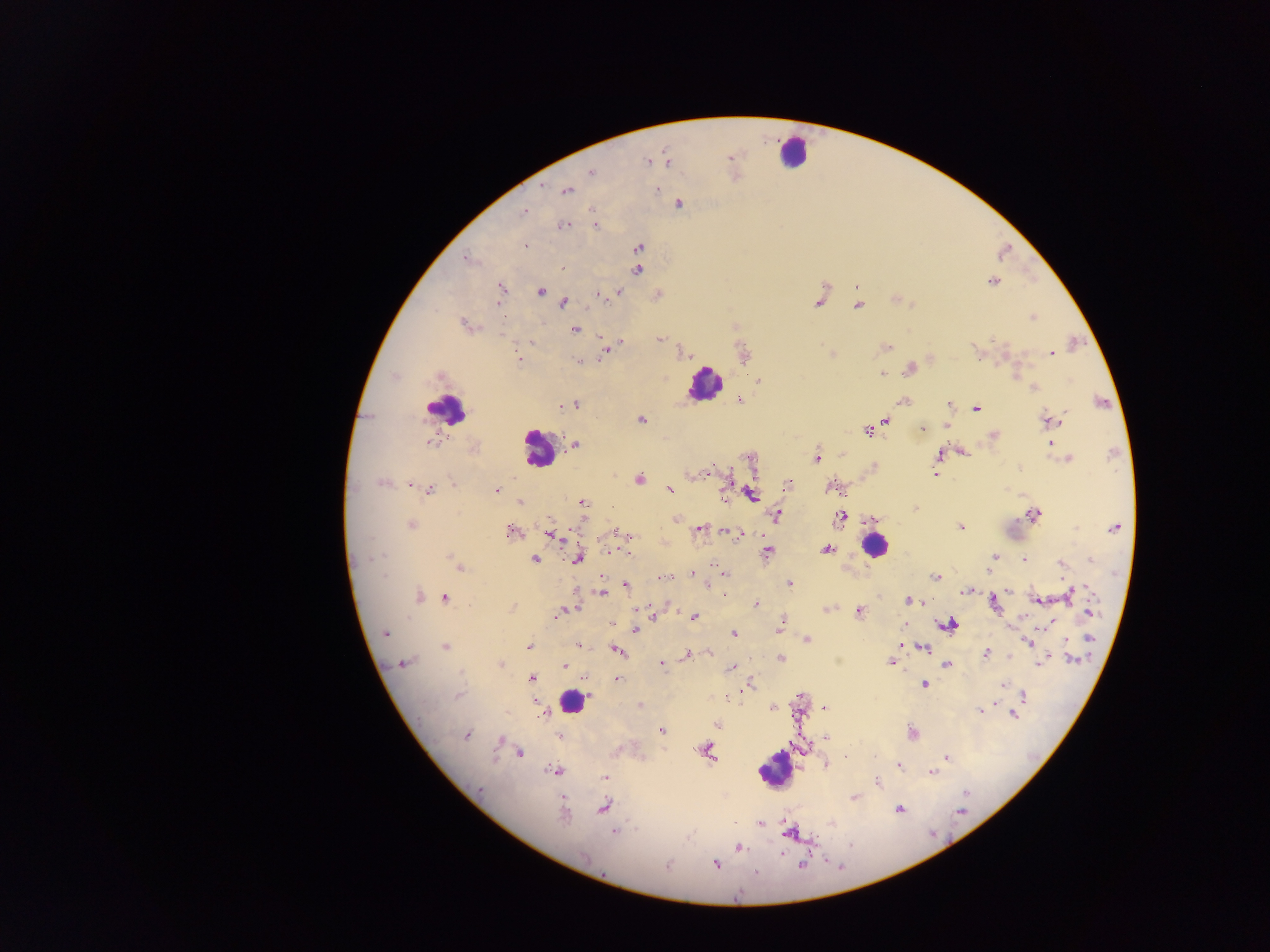
Approximate centers as [x, y] in pixels.
Summary:
  - Leukocyte locations: [792, 151], [704, 383], [446, 409], [537, 450], [874, 545], [572, 702], [775, 769]
  - Plasmodium parasite locations: [729, 159], [647, 161], [667, 162], [592, 172], [567, 190], [657, 190], [679, 204], [593, 210], [524, 213], [564, 225], [595, 225], [526, 246], [639, 247], [466, 260], [562, 268], [637, 270], [993, 282], [502, 288], [540, 292], [618, 293], [598, 295], [818, 301], [498, 302], [563, 302], [858, 305], [1032, 318], [465, 324], [575, 329], [599, 337], [659, 339], [621, 343], [885, 348], [606, 350], [976, 351], [683, 352], [1052, 353], [830, 354], [519, 359], [579, 362], [910, 369], [882, 374], [439, 376], [758, 381], [1033, 388], [741, 401], [902, 401], [1101, 402], [574, 404], [949, 405], [561, 406], [976, 408], [641, 419], [887, 420], [1050, 420], [922, 428], [867, 431], [993, 436], [431, 442], [574, 444], [964, 452], [938, 454], [817, 459], [1067, 459], [752, 462], [1018, 468], [933, 473], [707, 474], [639, 479], [382, 483], [453, 483], [789, 483], [411, 485], [832, 487], [496, 490], [670, 490], [430, 491], [725, 495], [751, 495], [583, 502], [520, 503], [914, 508], [1033, 514], [775, 515], [839, 518], [676, 520], [412, 524], [961, 527], [1114, 528], [699, 529], [511, 532], [729, 532], [620, 534], [736, 534], [553, 535], [826, 549], [611, 551], [627, 552], [767, 552], [382, 556], [994, 557], [450, 558], [577, 559], [535, 560], [1024, 560], [1091, 560], [1061, 564], [459, 568], [692, 574], [726, 576], [663, 577], [936, 577], [789, 584], [626, 585], [965, 591], [601, 593], [1070, 594], [418, 596], [445, 598], [1037, 599], [908, 601], [994, 603], [755, 604], [638, 607], [512, 608], [571, 609], [826, 609], [859, 612], [1090, 613], [559, 614], [653, 617], [694, 618], [610, 623], [949, 625], [779, 629], [635, 630], [385, 633], [733, 634], [1089, 638], [807, 639], [1027, 642], [529, 645], [578, 645], [446, 647], [923, 648], [618, 651], [986, 653], [687, 655], [780, 659], [1072, 660], [403, 663], [891, 663], [662, 664], [1041, 664], [501, 665], [947, 665], [565, 666], [732, 667], [531, 678], [584, 678], [617, 679], [924, 685], [1004, 685], [749, 686], [1024, 695], [639, 705], [772, 707], [824, 707], [981, 711], [1013, 714], [541, 715], [663, 731], [911, 733], [467, 735], [559, 736], [826, 738], [500, 740], [707, 750], [520, 753], [845, 756], [947, 758], [827, 765], [899, 765], [554, 770], [932, 772], [604, 777], [877, 782], [481, 790], [854, 797], [604, 807], [900, 810], [961, 810], [563, 814], [759, 823], [615, 832], [791, 833], [738, 847], [583, 857], [715, 864], [668, 865], [801, 865], [756, 872], [738, 894]
  - Capture: mobile-phone photograph through a microscope
  - Image size: 1270×952 pixels
  - Preparation: thick blood film
  - Country: Ghana
  - Field of view: single